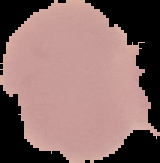

image type = segmented cell region on a black background
result = no malaria parasites seen
image size = 160×163 pixels
preparation = thin blood film